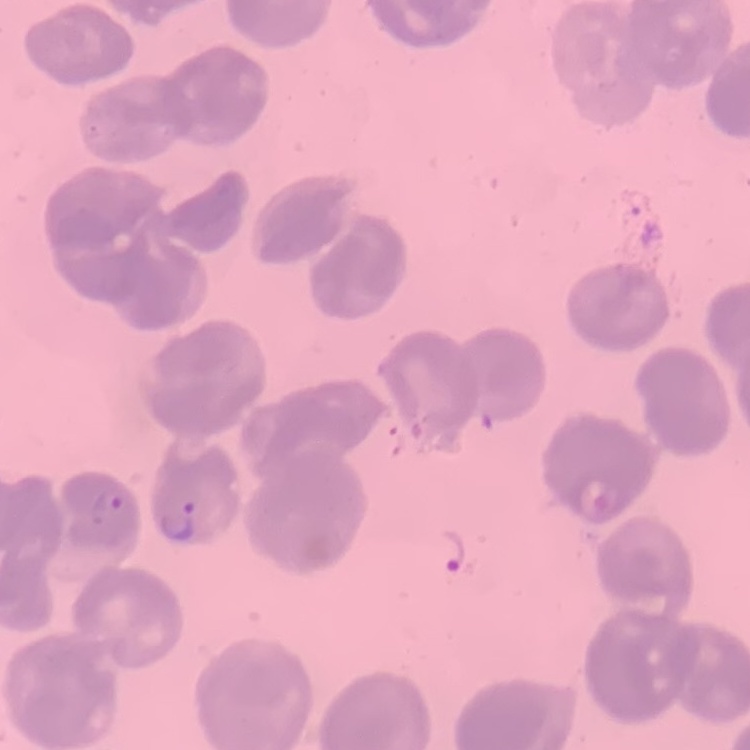

erythrocyte morphology = no rouleaux formation
stain = Field's or Giemsa
preparation = thin blood film
image type = square crop of a larger photomicrograph